Give the position of every Plasmodium parasite visible.
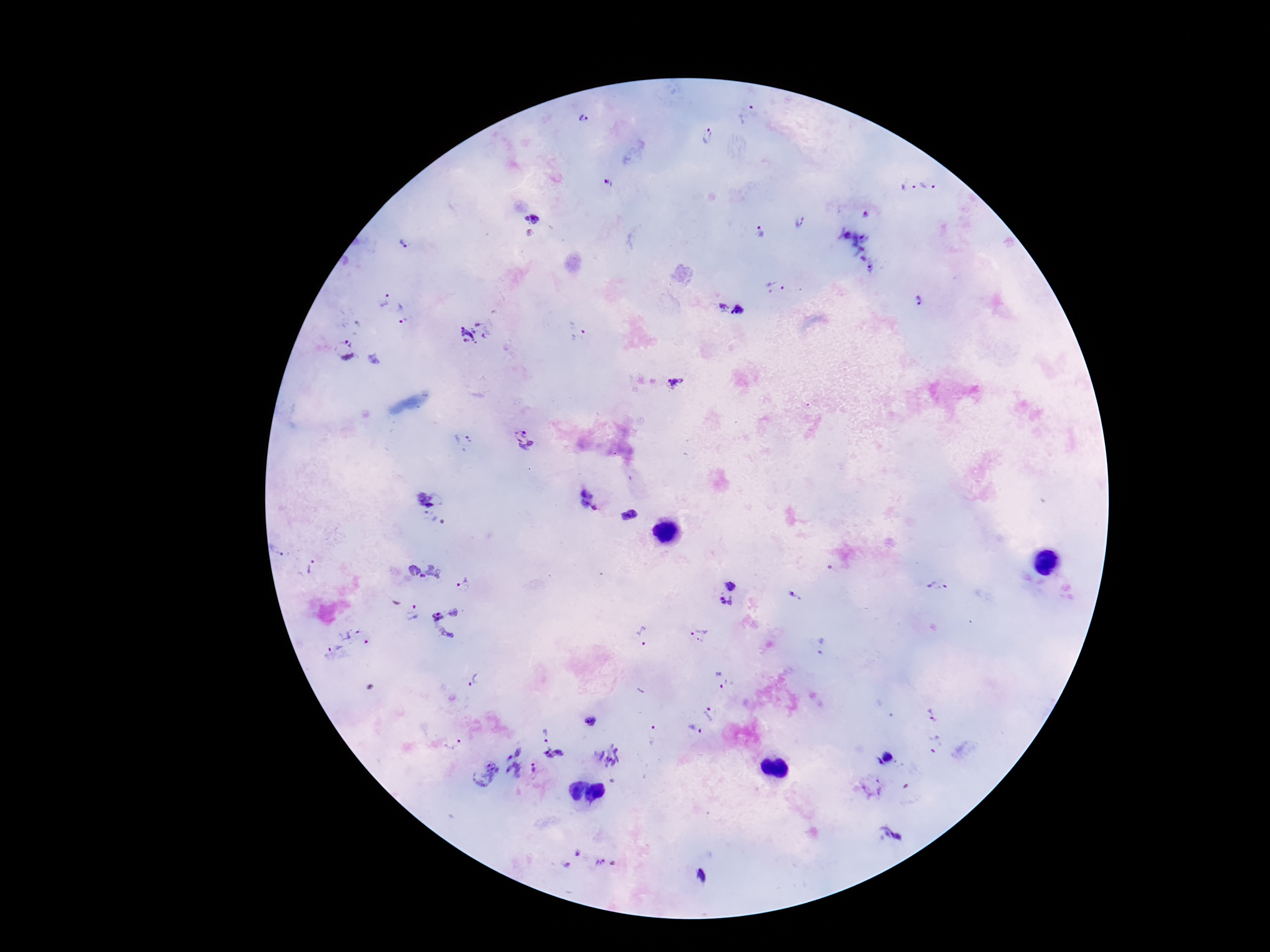

Approximate object centers, in pixels from the top-left corner.
Plasmodium parasites: (x=747, y=113), (x=583, y=119), (x=706, y=136), (x=608, y=183), (x=907, y=183), (x=934, y=183), (x=866, y=215), (x=531, y=218), (x=800, y=222), (x=530, y=233), (x=759, y=233), (x=405, y=244), (x=850, y=253), (x=775, y=288), (x=383, y=299), (x=921, y=300), (x=731, y=308), (x=401, y=313), (x=474, y=332), (x=576, y=332), (x=344, y=349), (x=673, y=384), (x=465, y=438), (x=525, y=439), (x=422, y=499), (x=437, y=500), (x=590, y=500), (x=427, y=514), (x=629, y=515), (x=438, y=520), (x=311, y=567), (x=436, y=570), (x=414, y=574), (x=938, y=584), (x=465, y=585), (x=731, y=587), (x=793, y=596), (x=722, y=602), (x=413, y=613), (x=446, y=621), (x=356, y=634), (x=699, y=636), (x=643, y=637), (x=821, y=646), (x=336, y=654), (x=721, y=680), (x=473, y=681), (x=709, y=713), (x=931, y=715), (x=591, y=722), (x=697, y=729), (x=654, y=734), (x=545, y=735), (x=935, y=742), (x=454, y=743), (x=555, y=755), (x=608, y=755), (x=886, y=759), (x=512, y=763), (x=534, y=769), (x=480, y=774), (x=871, y=788), (x=890, y=833), (x=578, y=853), (x=606, y=864), (x=565, y=867).

field of view = one from this slide
preparation = thick peripheral-blood smear
image size = 1270×952 pixels
stain = Giemsa
magnification = 100x
capture = smartphone camera through the microscope eyepiece
patient malaria status = positive